Assess this cell for malaria.
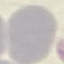
Uninfected.

Acquired by smartphone through the microscope eyepiece. Cell patch, automatically extracted from a larger field of view and resized to 64 × 64 pixels. Giemsa-stained preparation. Thin blood smear.